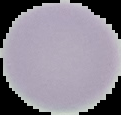

Image is 121×115 pixels. The area outside the segmented cell region is set to black. Malaria status: uninfected. From a thin blood smear.